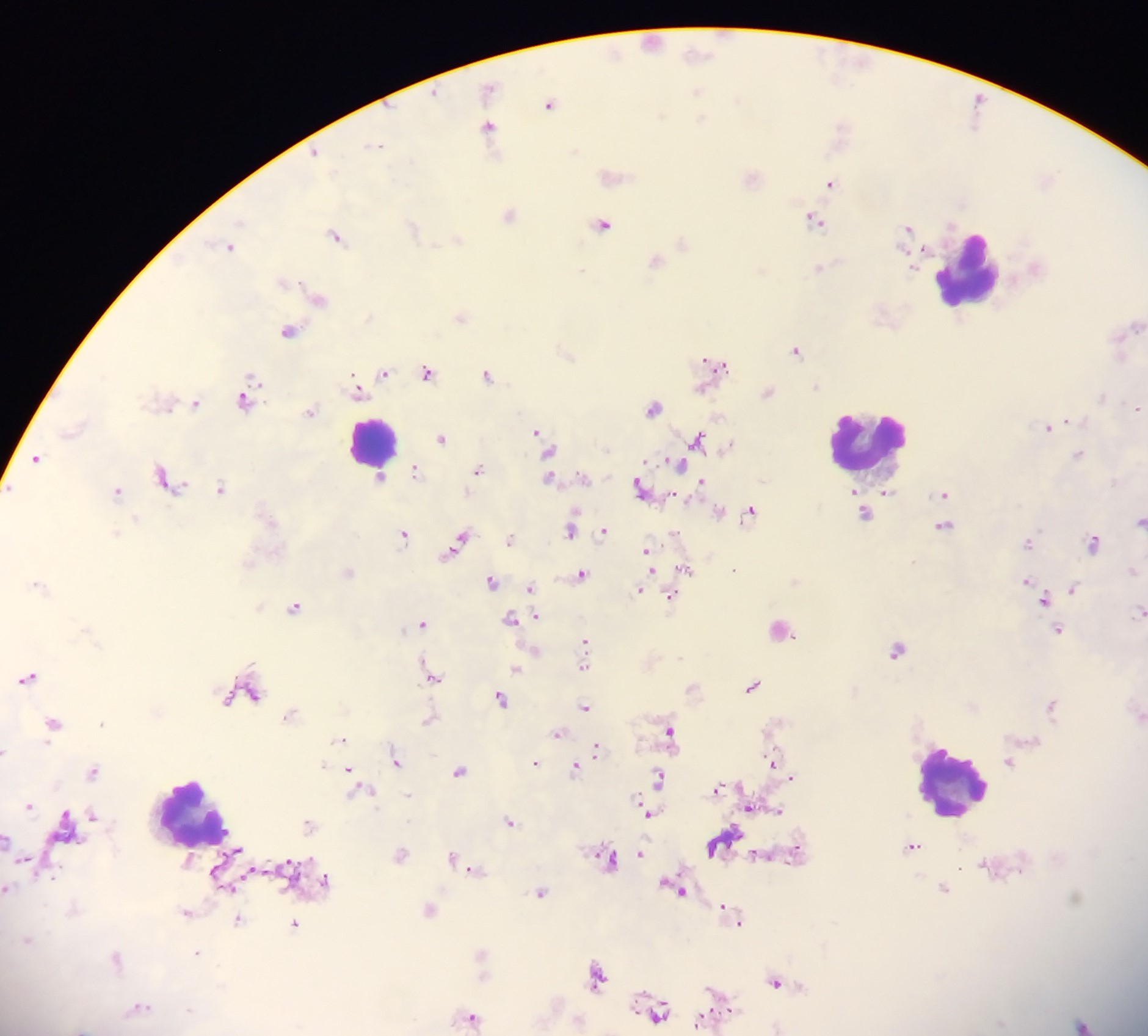

{
  "country": "Ghana",
  "leukocyte_locations": "approximate centers as {x, y} in pixels: {969, 269}, {882, 444}, {374, 447}, {954, 782}, {195, 817}",
  "preparation": "thick blood film",
  "capture": "mobile-phone photograph through a microscope",
  "plasmodium_parasite_locations": "approximate centers as {x, y} in pixels: {653, 41}, {698, 54}, {616, 55}, {490, 89}, {698, 91}, {738, 101}, {550, 104}, {702, 119}, {489, 127}, {375, 145}, {575, 151}, {315, 152}, {830, 183}, {510, 216}, {815, 219}, {602, 224}, {909, 227}, {412, 229}, {335, 236}, {459, 239}, {229, 246}, {656, 260}, {581, 271}, {320, 299}, {461, 315}, {1136, 325}, {290, 331}, {797, 350}, {717, 364}, {428, 372}, {384, 373}, {488, 376}, {706, 382}, {251, 387}, {359, 392}, {768, 392}, {1102, 397}, {246, 399}, {196, 404}, {653, 407}, {1137, 408}, {311, 411}, {1050, 427}, {536, 431}, {441, 438}, {699, 439}, {549, 452}, {1080, 455}, {37, 459}, {679, 464}, {478, 469}, {417, 472}, {380, 477}, {168, 479}, {550, 479}, {702, 483}, {639, 487}, {221, 488}, {887, 490}, {117, 492}, {944, 494}, {751, 511}, {719, 512}, {863, 514}, {1139, 522}, {945, 526}, {570, 530}, {604, 530}, {404, 535}, {510, 539}, {460, 540}, {1027, 543}, {1094, 543}, {648, 555}, {686, 569}, {582, 573}, {649, 574}, {491, 582}, {1027, 582}, {1073, 588}, {530, 589}, {640, 590}, {671, 597}, {1043, 599}, {295, 607}, {1138, 612}, {536, 617}, {511, 619}, {423, 623}, {780, 630}, {1058, 631}, {585, 642}, {898, 649}, {584, 666}, {516, 668}, {28, 677}, {434, 677}, {754, 686}, {247, 693}, {254, 694}, {501, 698}, {1052, 705}, {585, 707}, {290, 715}, {428, 721}, {53, 723}, {101, 723}, {669, 731}, {558, 734}, {340, 739}, {596, 749}, {5, 752}, {397, 761}, {773, 761}, {1010, 761}, {535, 764}, {575, 770}, {459, 771}, {93, 772}, {350, 772}, {660, 777}, {792, 778}, {353, 779}, {361, 789}, {718, 789}, {29, 806}, {751, 808}, {778, 810}, {649, 813}, {92, 816}, {510, 822}, {309, 825}, {8, 840}, {913, 846}, {796, 850}, {236, 851}, {640, 854}, {401, 855}, {454, 859}, {24, 860}, {609, 860}, {472, 869}, {325, 880}, {230, 888}, {676, 888}, {944, 889}, {8, 890}, {541, 892}, {1076, 897}, {430, 911}, {186, 912}, {730, 912}, {238, 920}, {737, 921}, {296, 924}, {27, 940}, {197, 954}, {482, 954}, {116, 959}, {600, 976}, {776, 982}, {139, 1007}, {657, 1012}, {471, 1018}, {707, 1018}, {1083, 1024}",
  "image_size": "1148×1036 pixels",
  "field_of_view": "single"
}